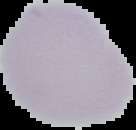

image type = segmented cell region on a black background
preparation = thin blood smear
image size = 136×130 pixels
result = no malaria parasites seen